Give the position of every malaria parasite.
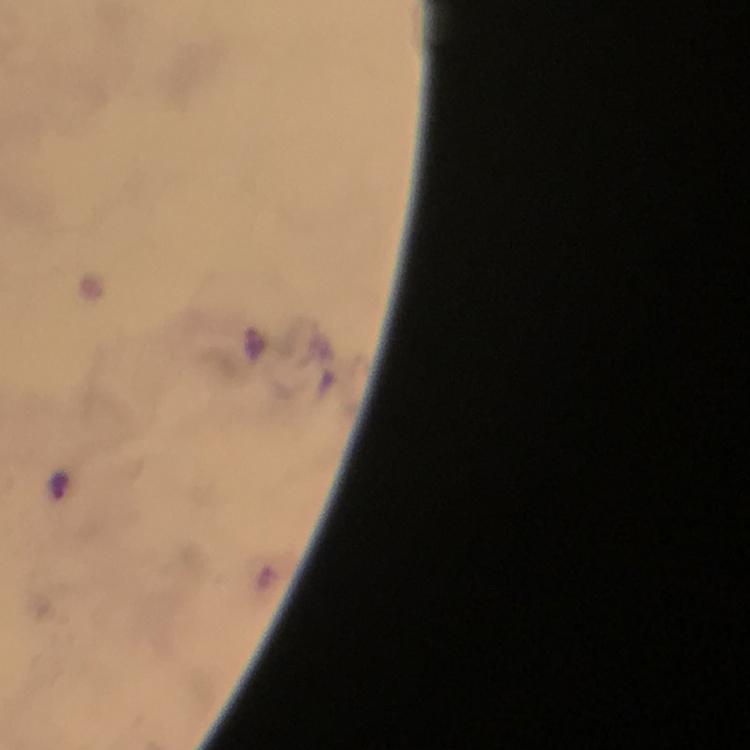

Approximate centers as (x, y) in pixels.
Malaria parasites: (60, 485).

Summary:
  - Preparation: thick blood film
  - Image size: 750×750 pixels
  - Magnification: 100x
  - Immersion oil: applied
  - Stain: Giemsa
  - Context: from a diagnostic examination for malaria
  - Cropped from: one field of view
  - Capture: smartphone mounted on the microscope